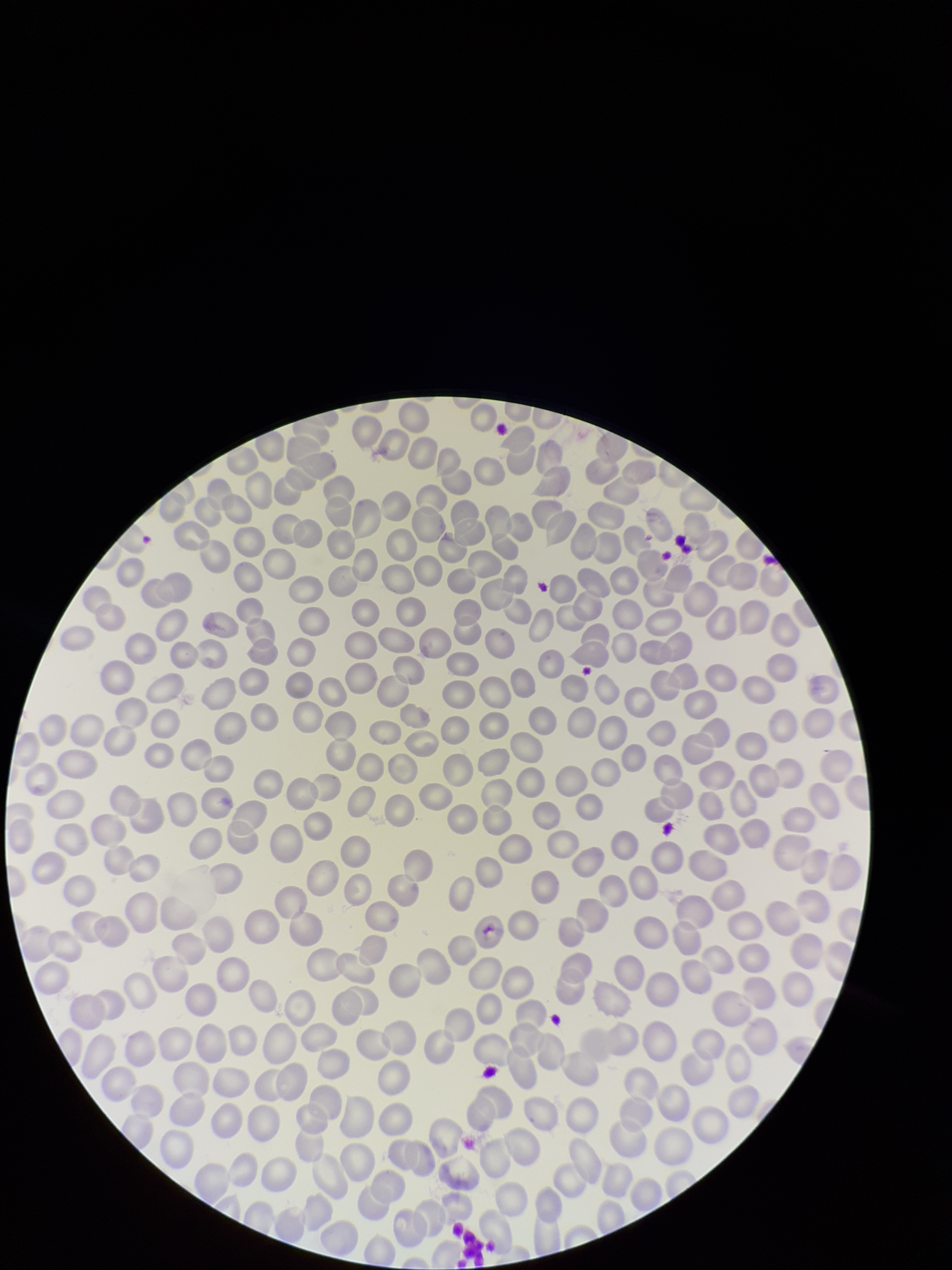
Patient malaria status: negative. Red blood cell count: 269. Parasitized red blood cell count: 0. Stained with Giemsa. Smartphone photograph taken through the eyepiece of a microscope. Preparation: thin. Parasitized red blood cells: none detected. Image is 952×1270 pixels. One field from this slide.